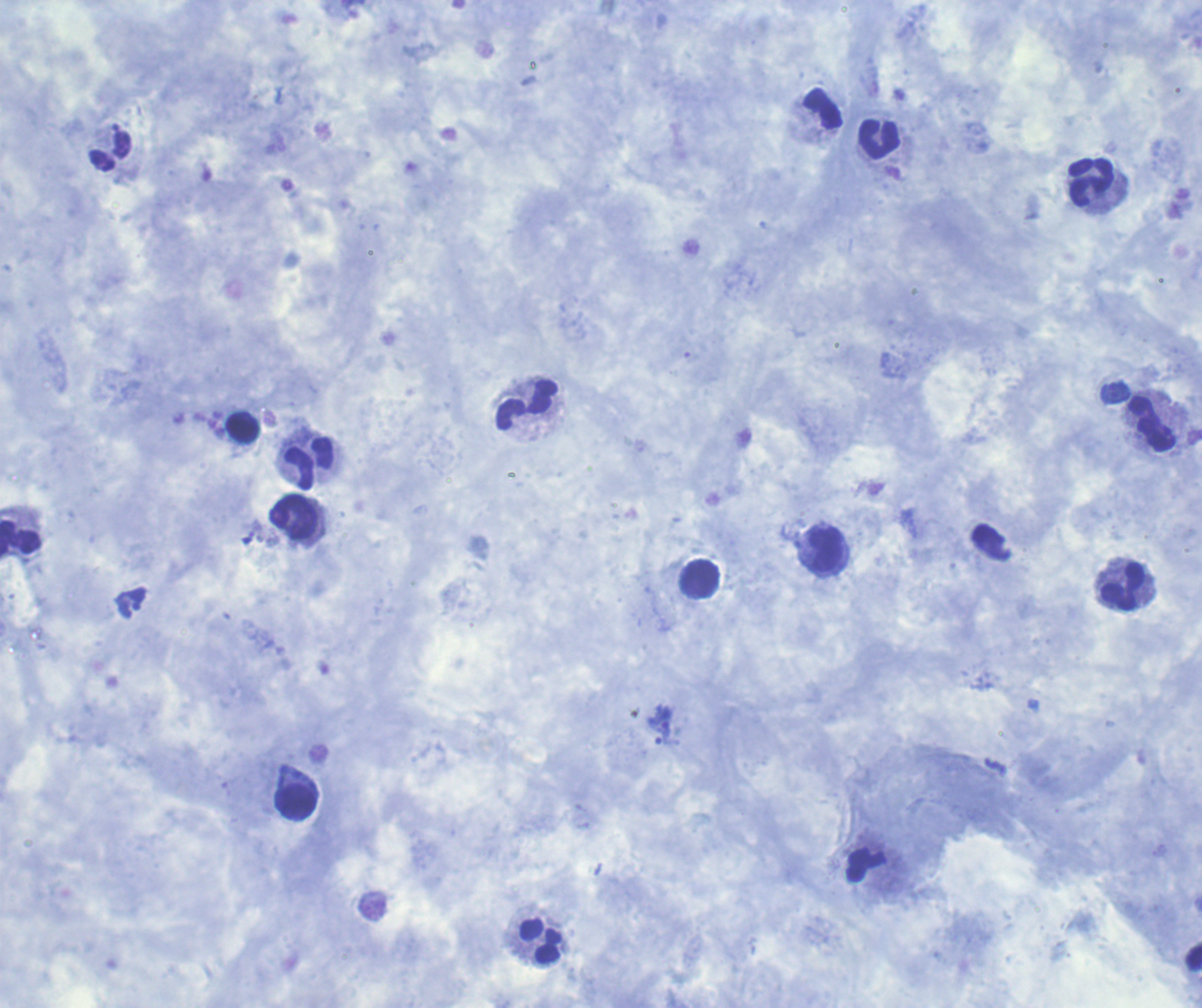

Approximate centers as {x, y} in pixels. Trophozoite locations: {660, 717}, {666, 737}. Leukocyte locations: {880, 140}, {1092, 183}, {529, 404}, {1152, 423}, {243, 428}, {310, 463}, {294, 518}, {20, 541}, {825, 551}, {700, 578}, {1123, 588}, {296, 801}, {541, 941}. Result: malaria parasites identified. Image is 1202×1008 pixels. Background quality: satisfactory. Single field of view. Previously used in a real diagnosis. Coloration quality: good. Romanowsky stain. 100x magnification. Thick blood smear.